State the preparation type.
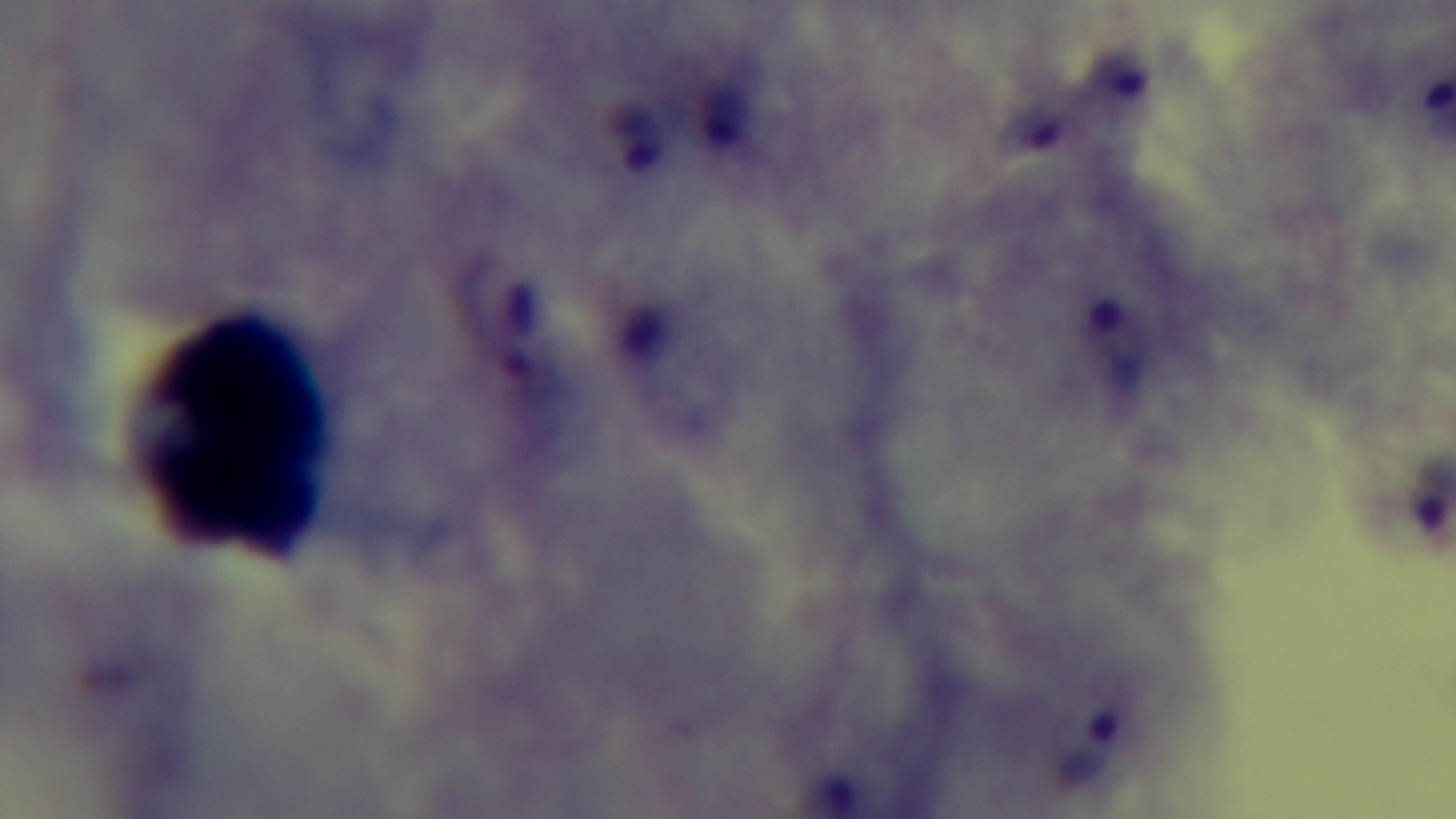

It is a thick blood film.

Summary:
  - Field of view: single
  - Malaria status: positive
  - Stain: Giemsa
  - Modality: light microscopy
  - Objective: 100x oil immersion
  - Capture: mounted 4K digital camera